Give the extent of all Plasmodium falciparum-infected red blood cells.
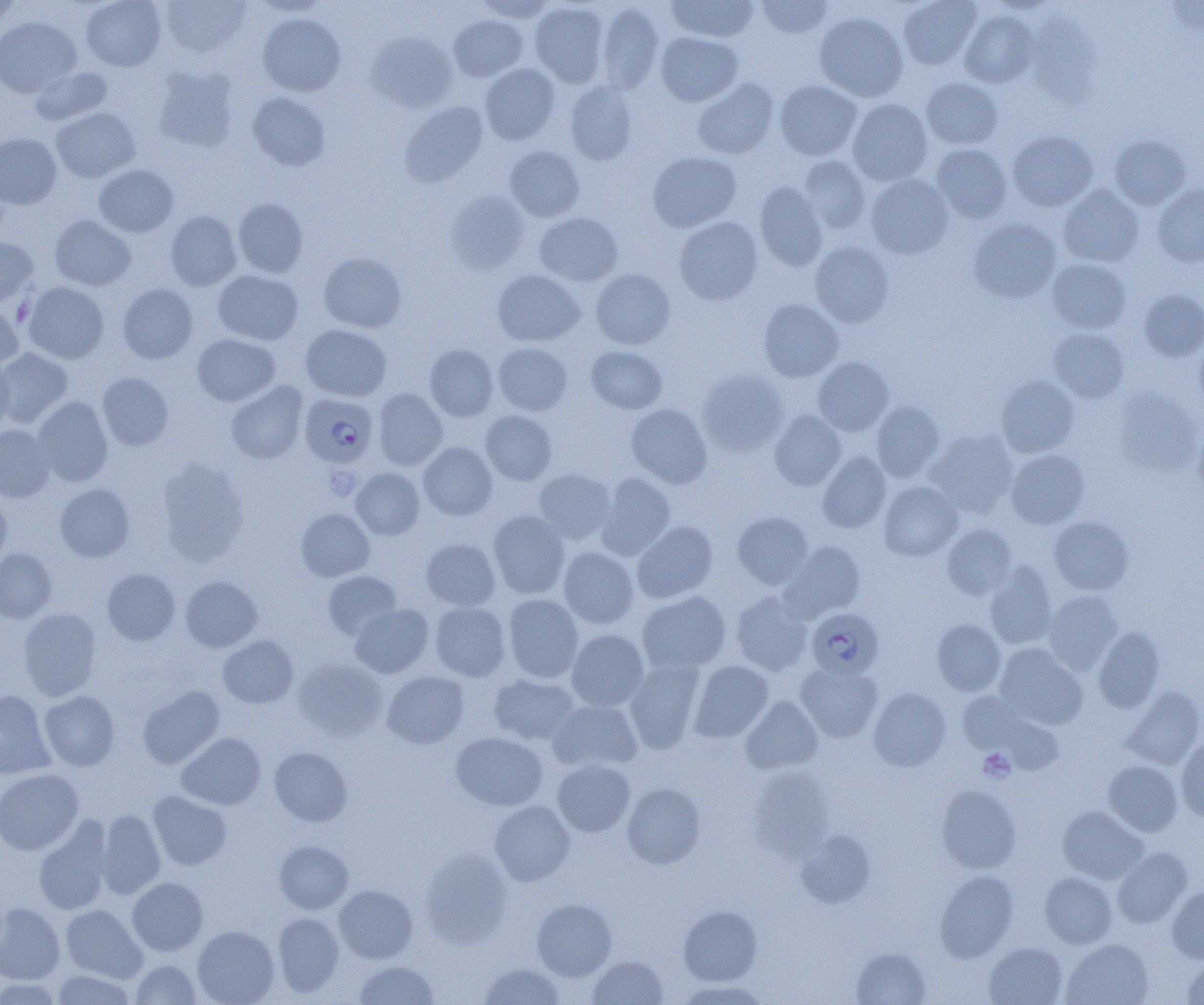
Approximate bounding boxes as (x1, y1, x2, y2) in pixels.
Plasmodium falciparum-infected red blood cells: (299, 393, 378, 468), (810, 611, 887, 683).

Platelet locations: (322, 466, 361, 501), (978, 749, 1016, 782). Uninfected red blood cell locations: (81, 0, 165, 71), (475, 0, 556, 23), (667, 0, 759, 42), (755, 0, 834, 39), (898, 0, 981, 69), (0, 1, 25, 26), (159, 1, 250, 57), (249, 1, 334, 17), (1165, 1, 1204, 37), (529, 2, 608, 88), (595, 2, 665, 94), (960, 10, 1038, 87), (814, 12, 908, 102), (257, 13, 345, 97), (449, 15, 529, 81), (1026, 15, 1100, 105), (0, 17, 81, 97), (365, 30, 458, 113), (655, 32, 743, 106), (152, 64, 240, 153), (480, 64, 561, 144), (30, 67, 113, 125), (921, 77, 1003, 150), (692, 78, 779, 160), (565, 80, 640, 165), (775, 80, 862, 160), (247, 92, 331, 171), (848, 98, 932, 185), (399, 101, 488, 187), (51, 107, 140, 183), (1007, 131, 1098, 212), (0, 133, 62, 209), (1110, 135, 1191, 210), (931, 144, 1012, 223), (505, 145, 584, 221), (648, 151, 742, 232), (798, 155, 871, 234), (93, 164, 178, 237), (865, 174, 953, 260), (755, 181, 827, 271), (1151, 184, 1204, 267), (1058, 185, 1144, 268), (445, 190, 530, 274), (233, 198, 308, 278), (166, 210, 242, 290), (534, 212, 623, 287), (50, 215, 136, 291), (674, 216, 763, 305), (968, 218, 1061, 303), (0, 237, 37, 307), (809, 241, 894, 327), (318, 253, 406, 333), (1047, 258, 1131, 333), (591, 269, 675, 349), (213, 270, 304, 345), (492, 270, 584, 346), (23, 281, 109, 363), (117, 284, 198, 364), (1138, 289, 1204, 361), (758, 299, 844, 382), (0, 304, 24, 369), (301, 324, 392, 401), (1049, 328, 1129, 403), (192, 334, 280, 406), (1194, 336, 1204, 412), (493, 342, 572, 416), (424, 344, 498, 421), (586, 345, 667, 414), (0, 348, 73, 427), (813, 357, 894, 436), (0, 358, 15, 431), (697, 369, 788, 456), (97, 372, 173, 450), (996, 376, 1079, 458), (226, 381, 308, 464), (1113, 387, 1201, 476), (374, 388, 447, 470), (32, 397, 113, 486), (871, 401, 944, 482), (626, 403, 712, 489), (480, 409, 557, 485), (769, 410, 846, 491), (0, 424, 55, 502), (927, 429, 1017, 517), (418, 442, 497, 520), (1006, 449, 1089, 528), (817, 452, 891, 533), (156, 460, 249, 566), (351, 467, 425, 539), (533, 469, 616, 545), (596, 473, 675, 559), (879, 481, 962, 561), (55, 484, 135, 561), (0, 496, 11, 566), (296, 508, 374, 581), (488, 511, 570, 598), (732, 512, 813, 589), (1049, 516, 1133, 594), (632, 521, 717, 603), (942, 524, 1017, 599), (421, 538, 500, 610), (781, 541, 865, 621), (558, 546, 639, 629), (0, 549, 56, 623), (984, 562, 1057, 649), (102, 569, 180, 645), (323, 571, 402, 640), (181, 576, 262, 652), (636, 591, 731, 673), (1043, 591, 1122, 673), (730, 592, 813, 675), (503, 594, 583, 682), (430, 602, 510, 681), (350, 603, 433, 678), (18, 608, 102, 701), (931, 619, 1006, 696), (1093, 627, 1165, 712), (566, 630, 649, 710), (217, 635, 298, 708), (994, 643, 1087, 729), (293, 657, 388, 740), (624, 658, 706, 753), (688, 660, 773, 743), (797, 663, 882, 742), (382, 670, 469, 748), (488, 673, 579, 745), (138, 685, 224, 769), (1123, 686, 1204, 770), (868, 688, 951, 772), (0, 690, 55, 779), (39, 690, 119, 771), (962, 692, 1062, 773), (740, 696, 823, 775), (547, 699, 642, 772), (451, 732, 548, 810), (176, 733, 266, 810), (1175, 736, 1204, 822), (269, 746, 352, 826), (552, 759, 635, 837), (1103, 760, 1182, 835), (750, 767, 834, 860), (0, 768, 83, 855), (622, 782, 706, 868), (936, 784, 1022, 874), (148, 791, 231, 870), (489, 801, 575, 885), (1057, 806, 1147, 884), (96, 809, 165, 899), (34, 817, 112, 916), (795, 830, 876, 907), (274, 841, 353, 913), (1113, 847, 1192, 928), (420, 850, 512, 947), (934, 870, 1018, 962), (1040, 872, 1117, 949), (127, 877, 207, 955), (334, 885, 417, 963), (1167, 886, 1204, 962), (532, 899, 616, 980), (0, 903, 64, 984), (61, 905, 147, 982), (679, 905, 762, 985), (272, 912, 344, 997), (192, 925, 279, 1005), (1061, 938, 1153, 1005), (984, 942, 1067, 1005), (851, 947, 930, 1005), (588, 955, 668, 1005), (1182, 958, 1204, 1004), (130, 959, 202, 1004), (354, 960, 439, 1005), (479, 963, 565, 1005), (51, 970, 136, 1004), (0, 978, 63, 1005), (674, 980, 771, 1005). Slide-level diagnosis: Plasmodium falciparum. One field of a larger specimen. Image is 1204×1005 pixels. 1000x magnification. Thin blood film. Optical microscopy.